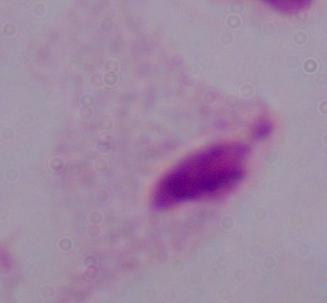

1000x magnification. A trichomonad is shown. Micrograph.